Report the malaria status of this cell.
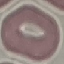

Uninfected.

preparation = thin blood film
stain = Giemsa
image type = automatically extracted cell patch, resized to 64 × 64 pixels
capture = smartphone through the microscope eyepiece